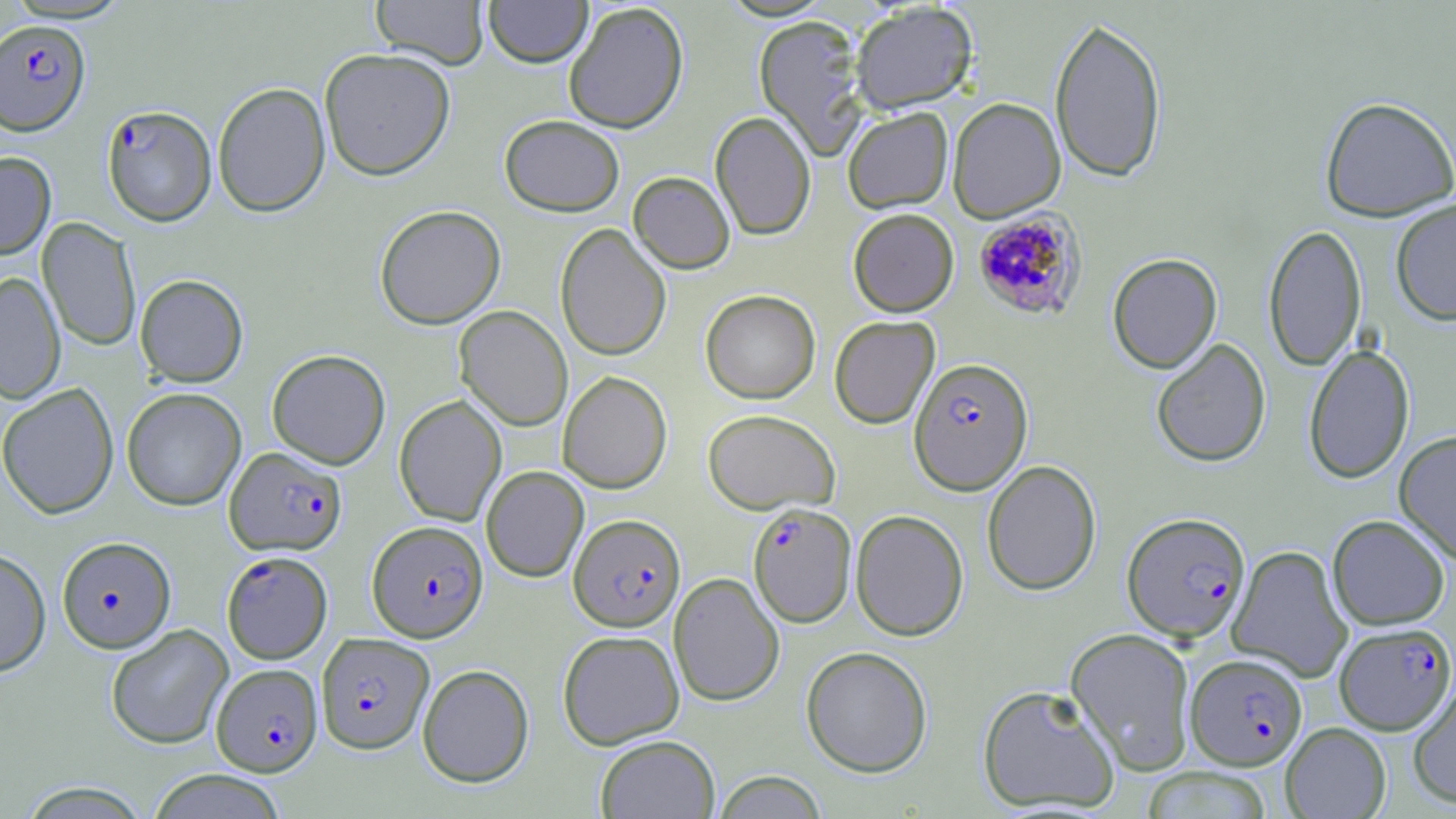

Approximate bounding boxes as (x1, y1, x2, y2) in pixels. Uninfected red blood cell locations: (371, 0, 489, 68), (483, 0, 593, 67), (563, 2, 689, 133), (850, 2, 978, 114), (753, 14, 869, 160), (1048, 15, 1168, 184), (319, 47, 456, 180), (212, 82, 331, 217), (948, 97, 1066, 223), (1319, 97, 1456, 221), (842, 107, 953, 213), (710, 111, 816, 240), (499, 114, 625, 216), (0, 151, 56, 260), (628, 171, 735, 273), (1390, 198, 1456, 326), (375, 204, 506, 329), (848, 208, 959, 316), (38, 217, 142, 352), (1263, 223, 1367, 373), (555, 224, 671, 360), (1107, 253, 1222, 373), (0, 272, 66, 404), (135, 274, 248, 386), (700, 290, 820, 404), (454, 305, 572, 431), (829, 315, 940, 429), (1151, 338, 1271, 468), (1303, 343, 1414, 484), (267, 349, 391, 469), (557, 371, 672, 494), (0, 383, 119, 519), (122, 387, 246, 511), (393, 395, 507, 526), (703, 409, 840, 515), (1394, 430, 1456, 564), (982, 460, 1102, 596), (481, 466, 588, 582), (850, 509, 969, 641), (1327, 514, 1451, 630), (1227, 545, 1353, 684), (0, 548, 51, 677), (668, 573, 784, 706), (105, 624, 233, 749), (1065, 627, 1197, 775), (557, 629, 684, 749), (801, 646, 933, 777), (418, 663, 534, 787), (1407, 677, 1456, 809), (977, 684, 1121, 813), (1281, 722, 1391, 818), (595, 734, 720, 819), (1141, 766, 1274, 819), (147, 769, 287, 818), (711, 771, 829, 818), (17, 781, 154, 819). Plasmodium falciparum-infected red blood cell locations: (0, 19, 90, 135), (102, 105, 217, 226), (972, 208, 1087, 321), (909, 357, 1034, 495), (225, 446, 346, 556), (748, 503, 856, 627), (1122, 512, 1251, 643), (569, 513, 685, 631), (368, 520, 488, 642), (57, 536, 176, 653), (221, 550, 332, 664), (1334, 622, 1456, 735), (316, 633, 434, 753), (1185, 653, 1307, 770), (211, 663, 322, 776). Slide-level diagnosis: Plasmodium falciparum. Thin blood film. 1000x magnification. Single field of view. May-Grünwald-Giemsa-stained preparation. Optical microscopy. Image is 1456×819 pixels.